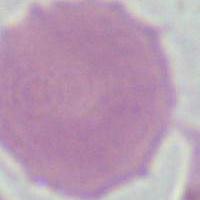
Summary:
  - Modality: photomicrograph
  - Identification: red blood cell
  - Magnification: 1000x